Assess this cell for malaria.
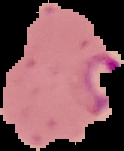

It is parasitized.

image type = cell region segmented out of the field of view; surrounding area masked to black
image size = 124×151 pixels
preparation = thin blood smear